State the blood parasite species.
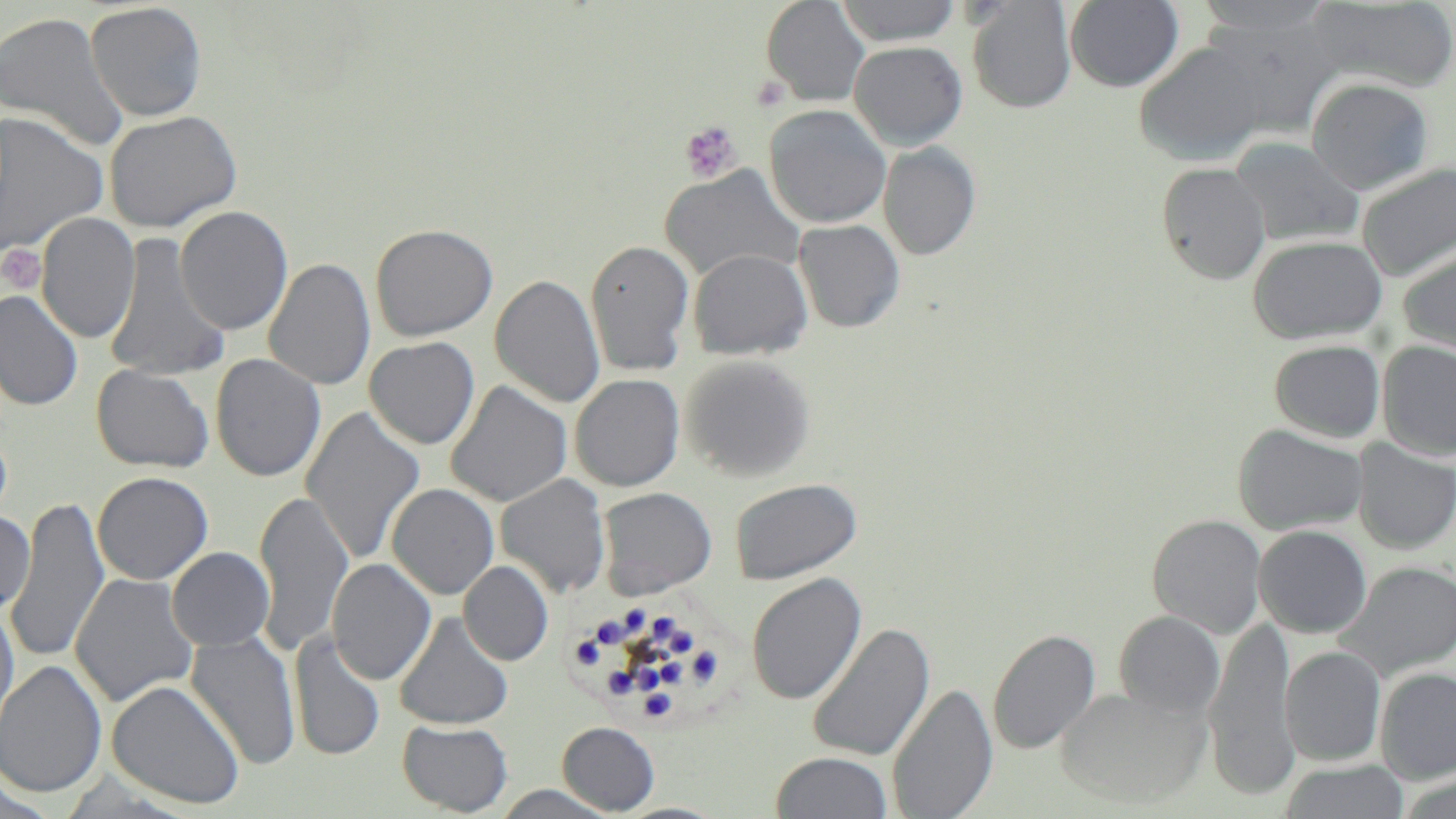

Plasmodium malariae.

Summary:
  - Coordinate format: approximate bounding boxes as (x1,y1)-(x2,y2) corner pairs in pixels
  - Uninfected red blood cell locations: (760,0)-(869,106), (967,0)-(1077,113), (1194,0)-(1337,42), (836,1)-(963,45), (1064,1)-(1183,92), (1304,1)-(1456,94), (86,2)-(207,121), (0,10)-(128,152), (848,40)-(968,150), (1133,41)-(1269,165), (1306,77)-(1433,194), (764,104)-(891,228), (104,110)-(242,233), (0,112)-(109,257), (1230,137)-(1364,248), (879,142)-(981,260), (1156,162)-(1271,285), (1356,162)-(1456,281), (659,165)-(805,283), (175,206)-(293,335), (36,212)-(140,344), (794,219)-(905,333), (370,223)-(498,341), (105,231)-(230,384), (1247,235)-(1388,344), (585,239)-(694,376), (1397,244)-(1456,361), (687,248)-(812,360), (264,258)-(376,391), (490,274)-(606,407), (0,289)-(84,411), (364,336)-(480,449), (1269,339)-(1385,443), (1377,339)-(1456,461), (210,353)-(326,482), (680,354)-(816,481), (91,364)-(214,473), (570,374)-(685,491), (446,382)-(572,507), (302,407)-(425,563), (1233,424)-(1368,535), (1352,439)-(1455,555), (92,471)-(213,585), (495,474)-(611,598), (729,477)-(862,585), (386,482)-(499,599), (597,487)-(717,599), (254,490)-(353,655), (4,500)-(110,663), (0,509)-(36,615), (1147,514)-(1267,638), (1253,525)-(1373,638), (167,547)-(274,651), (326,558)-(436,685), (458,560)-(554,666), (1337,561)-(1456,681), (70,572)-(197,708), (746,573)-(867,704), (0,602)-(20,744), (1113,611)-(1225,719), (394,612)-(513,730), (1202,615)-(1300,801), (806,623)-(935,762), (988,628)-(1101,754), (289,630)-(385,761), (185,631)-(301,771), (1280,646)-(1386,765), (0,660)-(107,797), (1375,668)-(1456,783), (106,679)-(246,809), (886,683)-(999,819), (1056,686)-(1212,808), (397,719)-(513,816), (557,721)-(659,814), (771,751)-(893,819), (1279,760)-(1410,819), (487,784)-(621,818), (612,802)-(729,819)
  - Plasmodium malariae-infected red blood cell locations: (567,601)-(725,727)
  - Platelet locations: (752,76)-(790,111), (680,120)-(743,185), (0,244)-(47,294)
  - Stain: May-Grünwald-Giemsa
  - Image size: 1456×819 pixels
  - Modality: optical microscopy
  - Field of view: one of a larger specimen
  - Preparation: thin blood film
  - Magnification: 1000x